Identify the parasite.
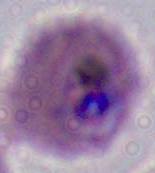
This is Plasmodium.

Summary:
  - Modality: micrograph
  - Magnification: 400x or 1000x